Assess the morphology of the red blood cells.
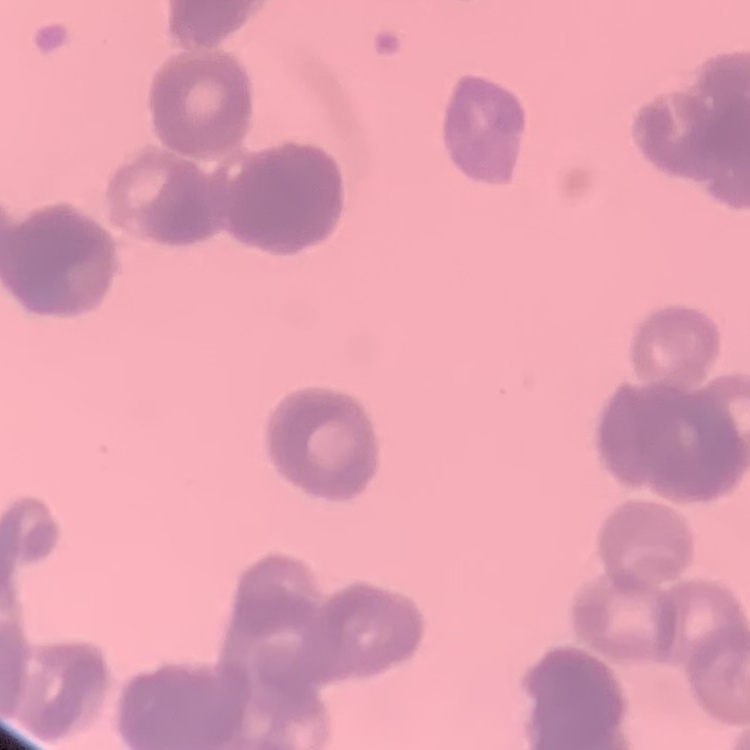

They show rouleaux formation.

Square crop of a larger photomicrograph. Thin blood film. Field's or Giemsa stain.